Outline each Plasmodium falciparum-infected red blood cell.
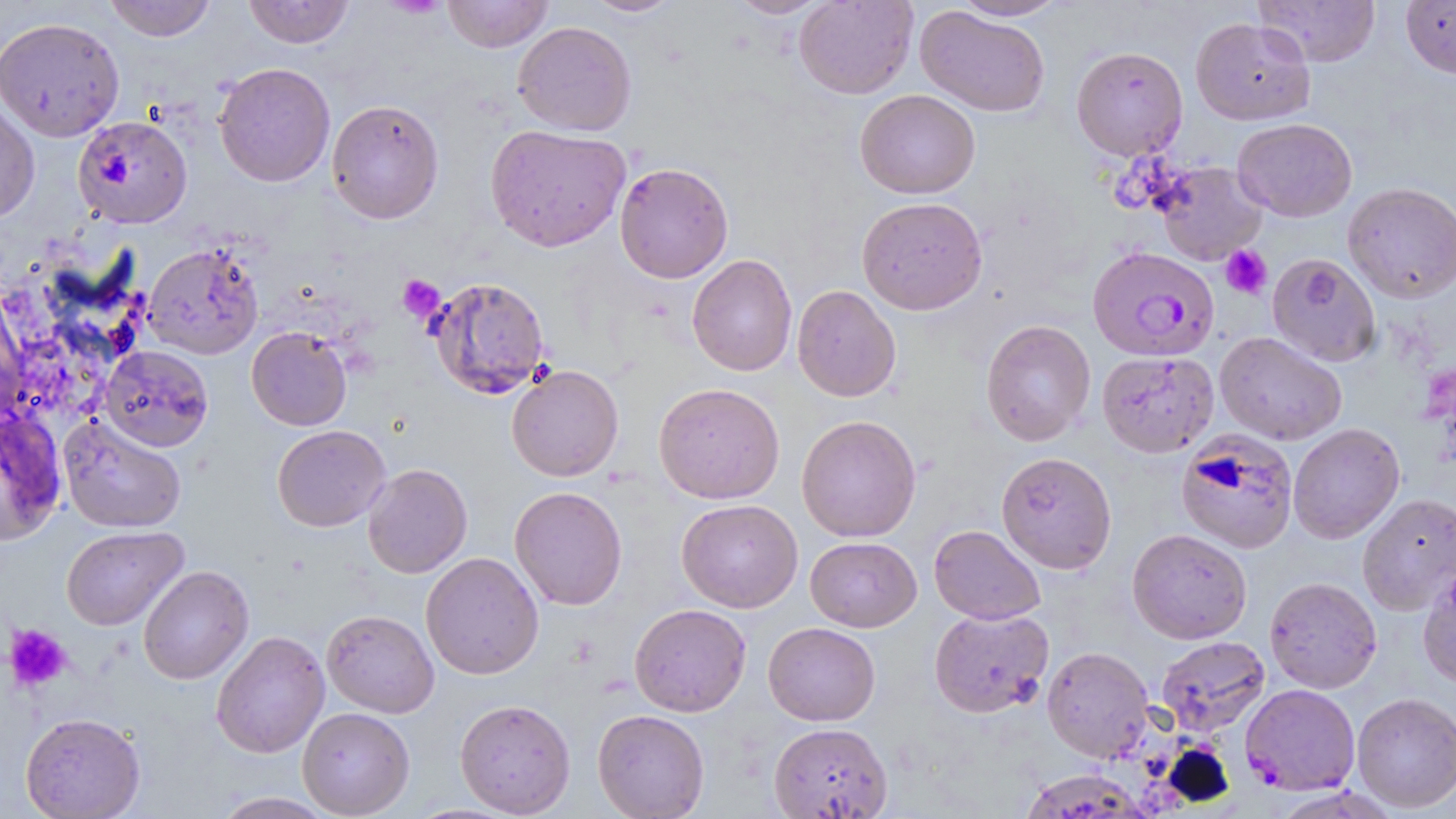

Approximate bounding boxes as (x1, y1, x2, y2) in pixels.
Plasmodium falciparum-infected red blood cells: (1087, 246, 1219, 361), (1240, 683, 1361, 796).

Summary:
  - Platelet locations: (1220, 245, 1272, 299), (397, 274, 445, 322), (4, 624, 73, 692)
  - Uninfected red blood cell locations: (104, 0, 217, 42), (242, 0, 356, 48), (441, 0, 555, 53), (582, 0, 684, 18), (728, 0, 831, 19), (794, 0, 917, 99), (951, 0, 1069, 21), (1253, 0, 1381, 67), (1401, 0, 1456, 78), (915, 6, 1050, 117), (0, 16, 125, 142), (1190, 17, 1315, 125), (513, 21, 637, 136), (1071, 45, 1188, 160), (213, 62, 336, 187), (855, 89, 980, 199), (0, 97, 40, 224), (327, 99, 445, 225), (74, 115, 192, 228), (1233, 118, 1357, 222), (485, 124, 631, 252), (1154, 161, 1268, 264), (614, 162, 733, 283), (1343, 182, 1456, 303), (857, 196, 988, 315), (143, 242, 264, 360), (1266, 253, 1381, 366), (687, 254, 797, 376), (426, 276, 550, 399), (792, 285, 901, 402), (0, 288, 33, 423), (980, 319, 1096, 446), (246, 326, 353, 431), (1215, 331, 1347, 445), (99, 345, 213, 452), (1096, 351, 1218, 458), (506, 364, 624, 482), (653, 382, 785, 504), (0, 410, 68, 545), (57, 414, 187, 533), (796, 415, 922, 542), (1288, 423, 1405, 544), (272, 424, 391, 532), (1175, 430, 1299, 555), (996, 451, 1117, 574), (362, 463, 473, 578), (509, 486, 628, 610), (1358, 493, 1456, 614), (676, 499, 803, 613), (928, 524, 1046, 624), (61, 525, 188, 631), (1127, 528, 1252, 644), (805, 536, 921, 632), (421, 552, 544, 679), (1418, 564, 1456, 689), (138, 565, 254, 685), (1264, 576, 1382, 693), (629, 603, 751, 717), (929, 608, 1054, 718), (322, 609, 439, 718), (763, 622, 880, 726), (210, 630, 330, 759), (1156, 635, 1270, 736), (1042, 646, 1155, 762), (1351, 692, 1456, 813), (454, 698, 576, 817), (297, 707, 415, 817), (592, 708, 710, 819), (20, 712, 146, 818), (768, 722, 893, 818), (1025, 768, 1152, 819), (213, 792, 337, 819)
  - Slide-level diagnosis: Plasmodium falciparum
  - Image size: 1456×819 pixels
  - Magnification: 1000x
  - Modality: optical microscopy
  - Preparation: thin blood film
  - Field of view: one of a larger specimen
  - Stain: May-Grünwald-Giemsa